Locate Plasmodium parasites and leukocytes.
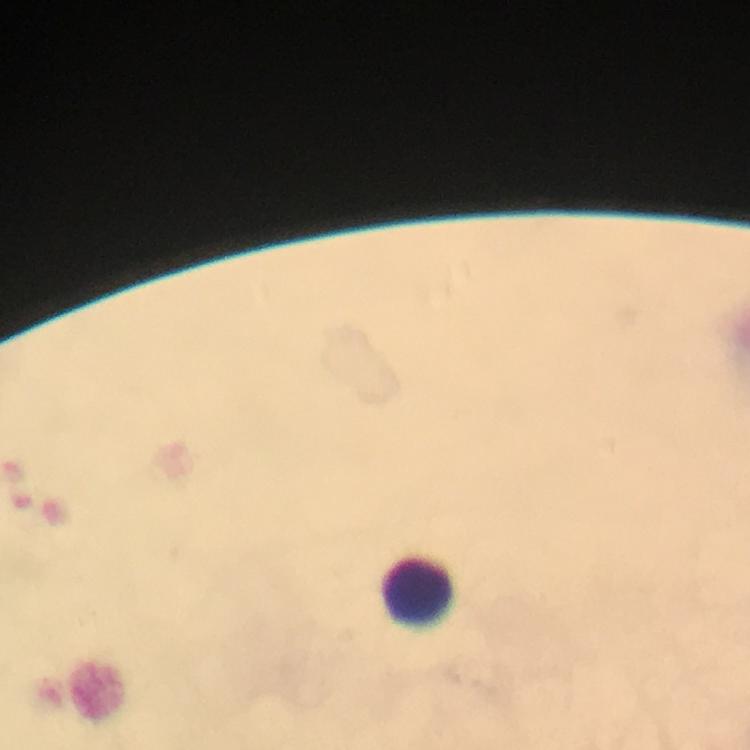

No Plasmodium parasites detected.
Approximate centers as [x, y] in pixels.
Leukocytes: [418, 590].

Thick blood film. Image is 750×750 pixels. Immersion oil was used. 100x magnification. From a malaria diagnostic workup. Giemsa-stained preparation. A crop from one field of view. Smartphone photograph taken through a microscope.